Name the blood parasite species.
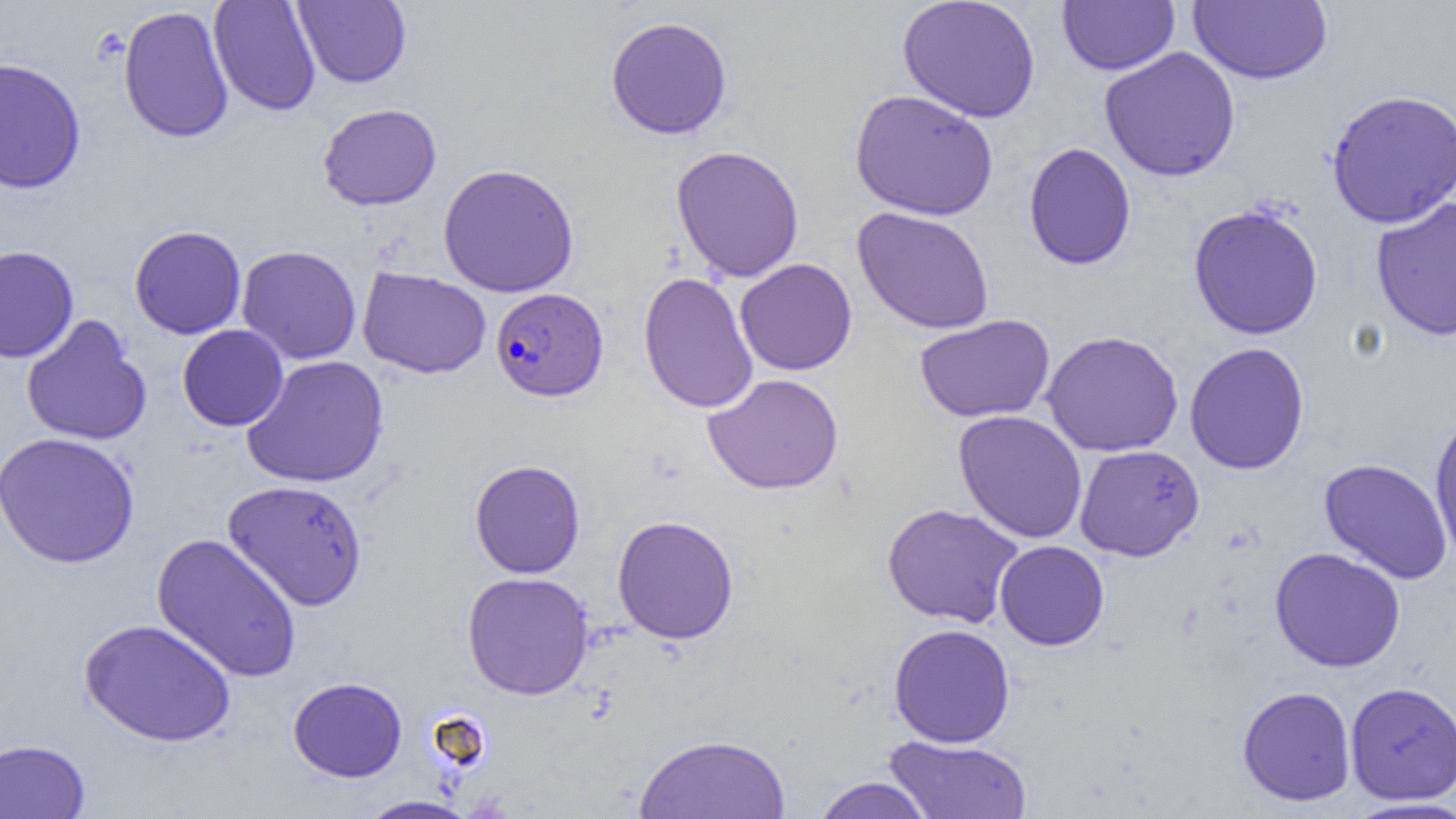

Plasmodium falciparum.

preparation = thin blood smear
Plasmodium falciparum-infected red blood cell locations = approximate bounding boxes as (x1, y1, x2, y2) in pixels: (491, 287, 609, 401)
uninfected red blood cell locations = approximate bounding boxes as (x1, y1, x2, y2) in pixels: (208, 0, 321, 116), (897, 0, 1041, 123), (293, 1, 412, 88), (1057, 1, 1179, 75), (1188, 1, 1333, 84), (117, 5, 234, 144), (605, 16, 733, 140), (1099, 46, 1240, 182), (0, 57, 87, 194), (1325, 88, 1456, 228), (849, 89, 998, 221), (317, 103, 442, 211), (1023, 142, 1137, 270), (670, 145, 805, 282), (437, 163, 579, 298), (1370, 196, 1456, 341), (1187, 204, 1324, 340), (851, 207, 995, 335), (129, 225, 246, 339), (0, 245, 79, 363), (236, 245, 362, 364), (735, 258, 858, 375), (357, 266, 492, 379), (638, 271, 758, 414), (914, 314, 1055, 423), (21, 315, 152, 447), (177, 324, 288, 431), (1041, 330, 1184, 457), (1184, 342, 1310, 475), (241, 355, 390, 488), (703, 373, 843, 495), (953, 410, 1088, 543), (1429, 410, 1456, 563), (0, 431, 140, 568), (1074, 444, 1204, 561), (1318, 458, 1453, 584), (469, 459, 586, 578), (223, 479, 368, 611), (881, 502, 1025, 628), (612, 515, 739, 644), (152, 533, 302, 682), (995, 540, 1109, 650), (1269, 547, 1406, 673), (462, 571, 594, 700), (79, 617, 236, 747), (888, 623, 1016, 747), (288, 677, 407, 782), (1344, 681, 1456, 805), (1237, 685, 1356, 807), (634, 733, 792, 818), (884, 735, 1033, 818), (0, 738, 91, 819), (812, 776, 935, 819), (357, 795, 478, 818), (1344, 797, 1456, 819)
modality = light microscopy
image size = 1456×819 pixels
field of view = single
magnification = 1000x